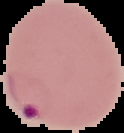
Image is 124×133 pixels. From a thin blood smear. Segmented cell region on a black background. Malaria status: parasitized.